Describe the morphology of the red blood cells.
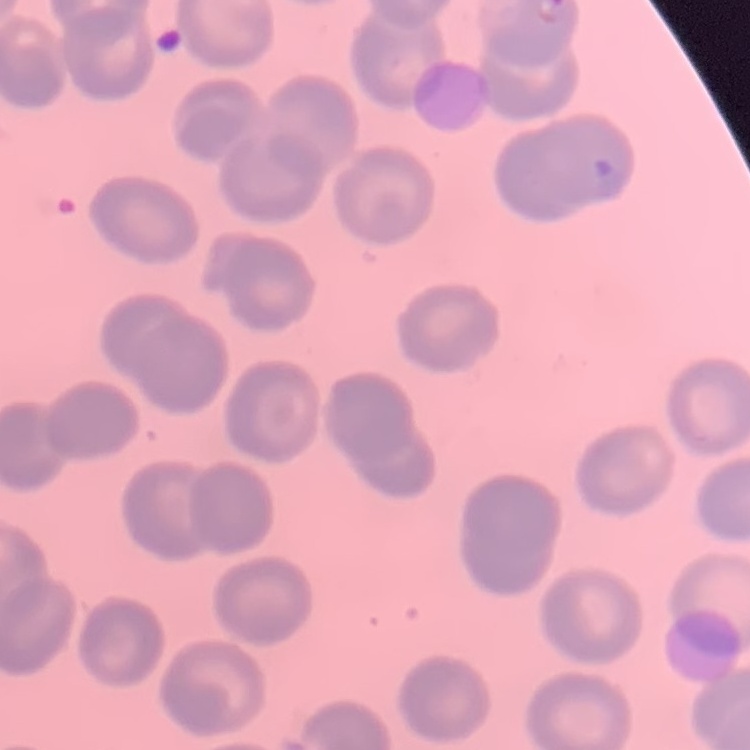
They show no rouleaux formation.

Summary:
  - Stain: Field's or Giemsa
  - Image type: square crop of a larger photomicrograph
  - Preparation: thin peripheral smear